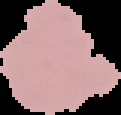

preparation = thin blood smear
image size = 121×115 pixels
image type = segmented cell region with the area outside set to black
result = no Plasmodium parasites seen